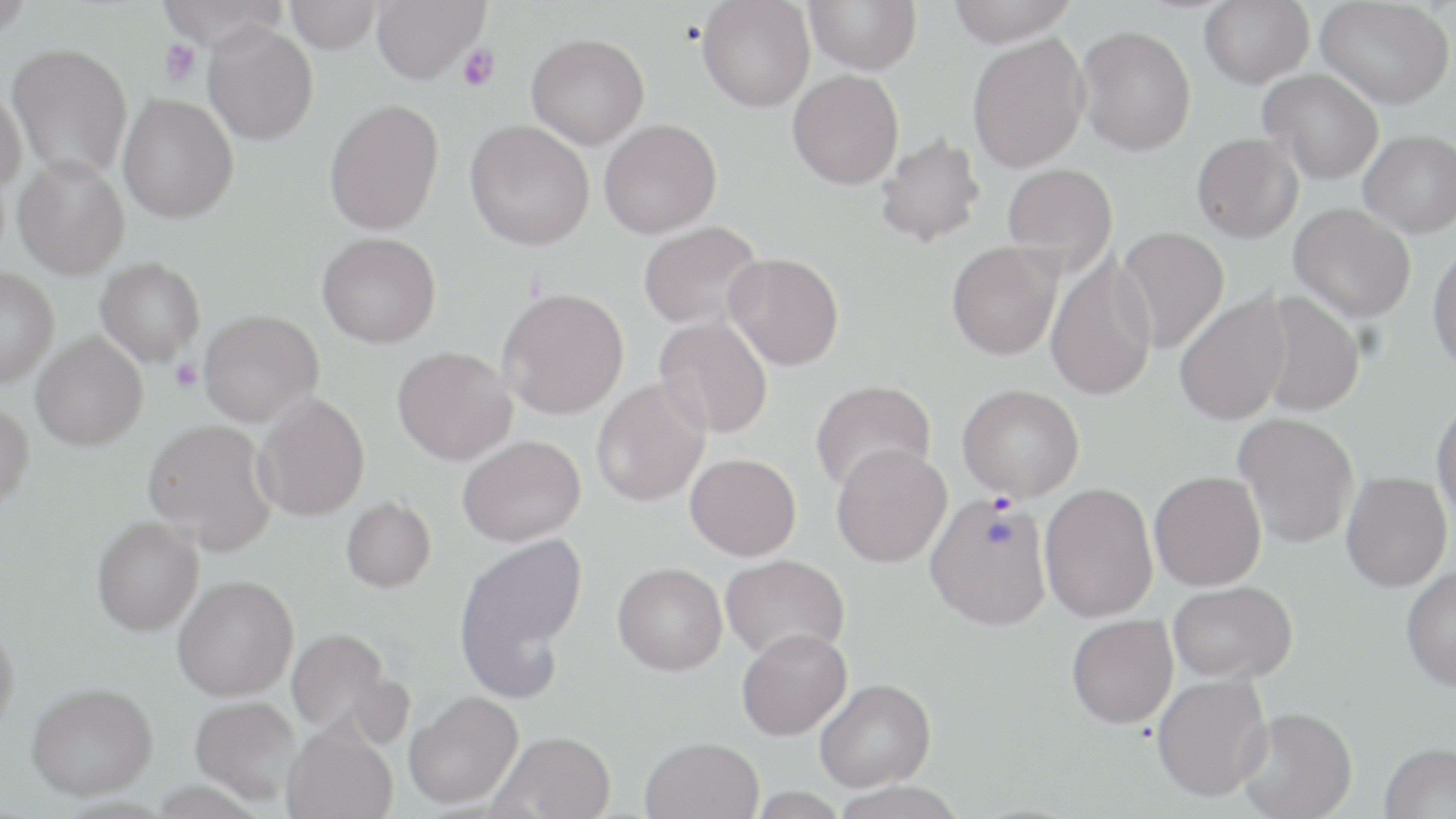 Approximate bounding boxes as (x1, y1, x2, y2) in pixels. Plasmodium vivax-infected red blood cell locations: (925, 494, 1052, 630). Platelet locations: (159, 38, 202, 87), (457, 44, 500, 92), (170, 360, 202, 392). Uninfected red blood cell locations: (0, 0, 35, 38), (155, 0, 288, 51), (285, 0, 382, 53), (372, 0, 488, 83), (805, 0, 922, 74), (946, 0, 1080, 46), (1199, 0, 1314, 88), (1317, 0, 1455, 109), (697, 1, 815, 112), (203, 22, 318, 145), (1076, 25, 1196, 155), (526, 33, 649, 148), (967, 33, 1089, 172), (6, 42, 132, 180), (1259, 69, 1384, 185), (787, 70, 904, 189), (0, 83, 27, 196), (118, 94, 238, 223), (324, 99, 444, 235), (599, 119, 721, 239), (465, 120, 594, 249), (1360, 129, 1456, 237), (1192, 132, 1302, 242), (874, 134, 986, 248), (12, 156, 129, 280), (1002, 162, 1118, 275), (1290, 203, 1416, 323), (638, 220, 763, 331), (1115, 227, 1229, 354), (316, 232, 441, 348), (947, 241, 1062, 360), (1428, 241, 1456, 374), (723, 252, 844, 370), (1045, 252, 1157, 401), (94, 258, 205, 368), (0, 269, 58, 389), (497, 288, 628, 419), (1251, 290, 1365, 418), (1174, 291, 1293, 427), (198, 310, 322, 427), (653, 315, 774, 439), (32, 335, 148, 454), (393, 348, 517, 466), (592, 378, 710, 507), (810, 379, 936, 496), (957, 383, 1084, 500), (254, 393, 370, 522), (1432, 399, 1456, 528), (0, 403, 34, 516), (1234, 412, 1360, 549), (143, 421, 276, 554), (457, 437, 586, 547), (831, 443, 952, 567), (685, 454, 801, 560), (1149, 470, 1267, 591), (1342, 471, 1453, 592), (1040, 482, 1158, 622), (341, 499, 435, 595), (91, 520, 203, 639), (459, 535, 587, 661), (721, 554, 850, 662), (612, 563, 727, 675), (1401, 565, 1456, 691), (173, 580, 298, 705), (1168, 581, 1297, 683), (456, 589, 568, 707), (1067, 614, 1178, 729), (0, 623, 19, 746), (736, 627, 852, 740), (286, 630, 392, 740), (1152, 674, 1272, 802), (815, 678, 936, 791), (26, 687, 158, 807), (405, 694, 524, 813), (190, 700, 302, 810), (1237, 706, 1357, 819), (281, 728, 399, 819), (490, 734, 616, 819), (641, 738, 764, 819), (1379, 743, 1455, 818). Slide-level diagnosis: Plasmodium vivax. Image is 1456×819 pixels. Light microscopy. Single field of view. Thin blood film. Captured at 1000x magnification. May-Grünwald-Giemsa-stained preparation.